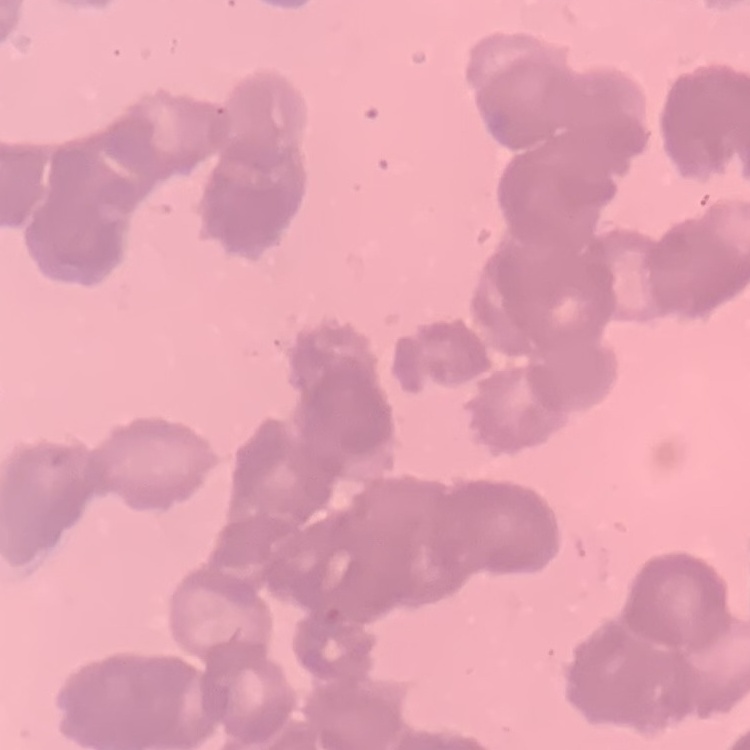

The red blood cells show rouleaux formation. One tile cut from a larger photomicrograph. Thin peripheral smear. Stained with either Field's or Giemsa.